Name the parasite shown.
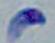

This is Toxoplasma gondii.

Summary:
  - Magnification: 1000x
  - Modality: micrograph